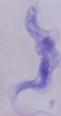

modality: micrograph
magnification: 1000x
identification: trypanosome